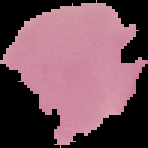

Result: no malaria parasites seen. From a thin blood film. Image is 148×148 pixels. The area outside the segmented cell region is set to black.